Assess the morphology of the red blood cells.
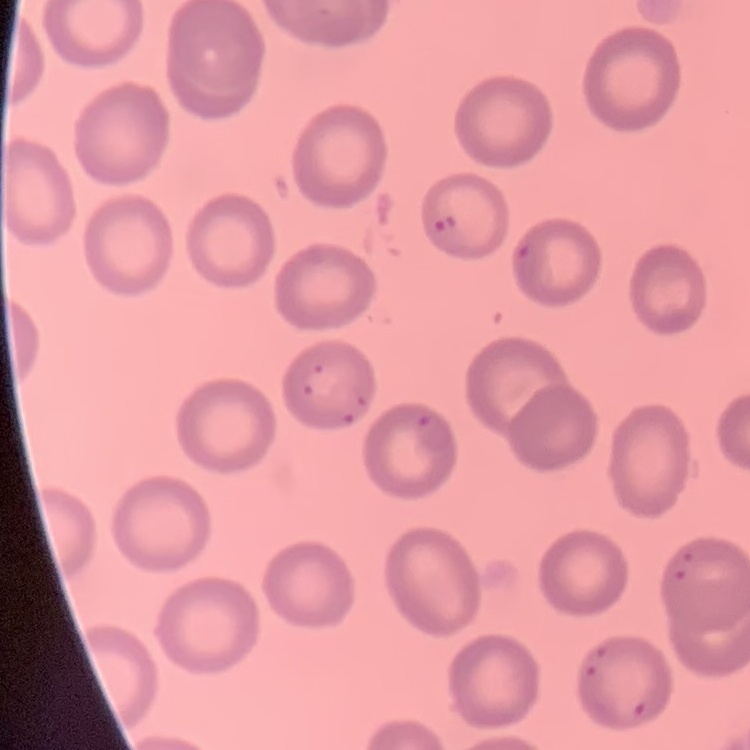
No rouleaux formation.

{
  "stain": "Field's or Giemsa",
  "image_type": "one tile cut from a larger photomicrograph",
  "preparation": "thin blood film"
}